Classify this cell by malaria status.
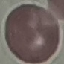

It is uninfected.

image type = automatically extracted cell patch, resized to 64 × 64 pixels
preparation = thin blood smear
stain = Giemsa
capture = smartphone through the microscope eyepiece